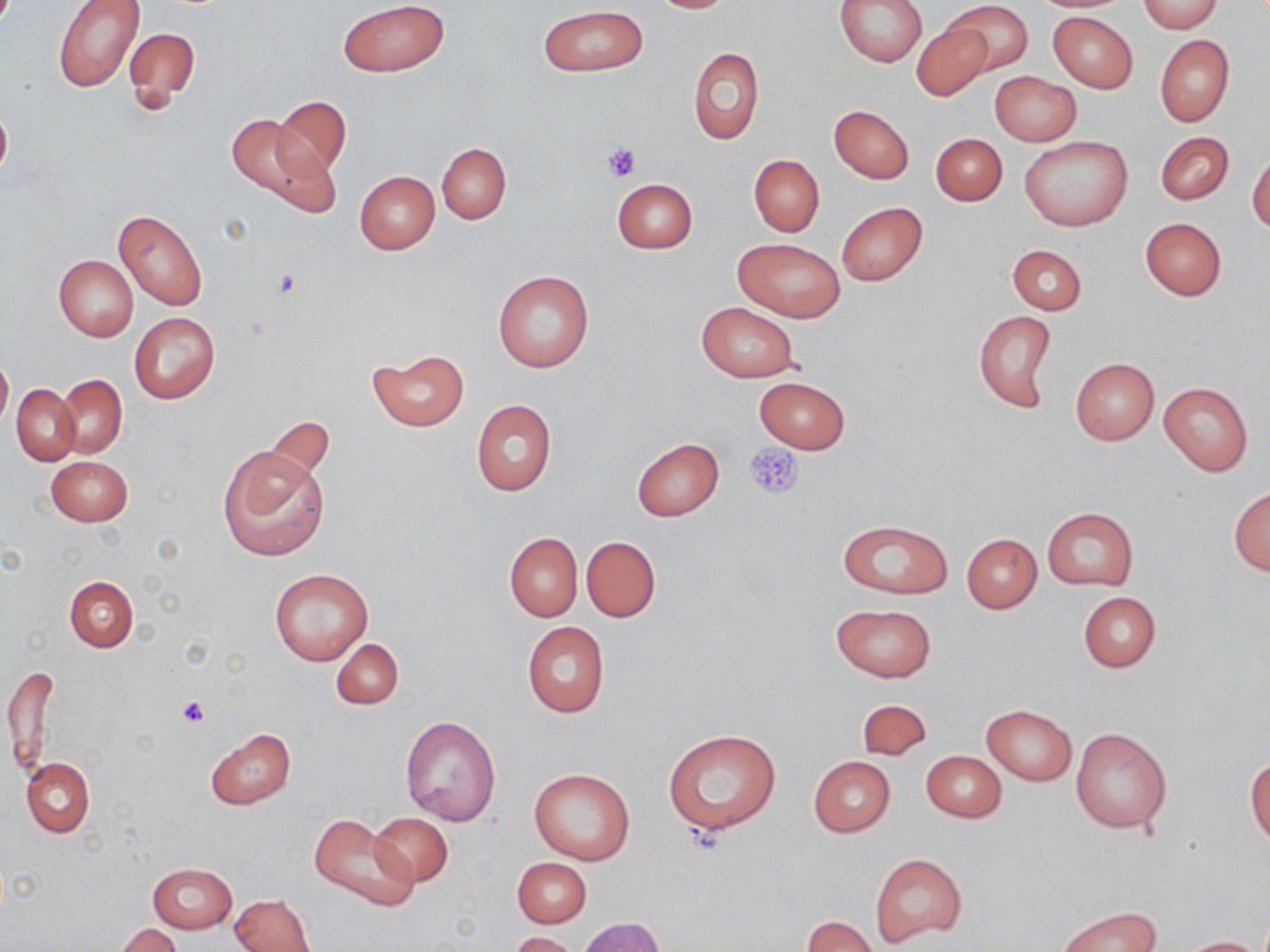

Summary:
  - Coordinate format: approximate bounding boxes as (x1,y1)-(x2,y2) corner pairs in pixels
  - Platelet locations: (602,143)-(642,183), (745,442)-(803,500), (177,695)-(209,729)
  - Uninfected red blood cell locations: (337,0)-(449,76), (648,0)-(738,13), (834,0)-(929,66), (940,0)-(1034,77), (1135,0)-(1222,33), (52,1)-(143,93), (539,5)-(646,77), (1048,11)-(1137,94), (911,21)-(995,101), (123,26)-(202,111), (1155,35)-(1234,127), (688,48)-(764,147), (990,71)-(1081,145), (272,95)-(351,178), (0,102)-(11,185), (829,104)-(914,183), (224,113)-(334,213), (1155,131)-(1233,205), (930,133)-(1008,207), (1020,136)-(1131,232), (437,144)-(510,223), (1247,148)-(1269,235), (749,154)-(824,237), (744,155)-(832,325), (354,171)-(440,254), (611,178)-(698,254), (837,201)-(928,286), (114,208)-(208,310), (1140,217)-(1226,300), (732,238)-(844,322), (1007,244)-(1087,315), (54,255)-(139,342), (492,270)-(594,372), (697,302)-(800,382), (973,309)-(1058,414), (129,312)-(219,403), (367,348)-(469,432), (0,352)-(12,433), (1070,358)-(1158,444), (56,375)-(127,457), (754,376)-(849,453), (1159,382)-(1252,475), (12,385)-(80,465), (471,399)-(557,496), (263,416)-(335,483), (631,438)-(724,520), (218,446)-(328,562), (46,454)-(132,527), (1228,487)-(1270,575), (1041,505)-(1138,591), (838,519)-(953,599), (504,532)-(583,621), (961,533)-(1042,612), (580,535)-(661,622), (268,567)-(374,666), (64,575)-(138,653), (1078,592)-(1160,672), (830,603)-(936,682), (522,622)-(609,717), (330,637)-(404,709), (4,662)-(59,774), (856,698)-(931,760), (982,704)-(1077,785), (400,714)-(501,826), (205,727)-(295,809), (1070,727)-(1172,833), (663,729)-(781,836), (921,751)-(1006,822), (809,756)-(895,836), (20,757)-(95,838), (1246,757)-(1270,846), (529,768)-(633,865), (367,811)-(455,888), (308,813)-(419,913), (870,853)-(966,947), (512,857)-(591,928), (148,862)-(237,933), (231,892)-(315,952), (1058,906)-(1159,952), (577,916)-(666,952), (801,916)-(877,952), (115,924)-(184,951), (509,931)-(579,952), (1179,936)-(1265,951)
  - Slide-level diagnosis: no evidence of blood parasites
  - Stain: May-Grünwald-Giemsa
  - Image size: 1270×952 pixels
  - Preparation: thin blood film
  - Field of view: one of a larger specimen
  - Modality: optical microscopy
  - Magnification: 1000x